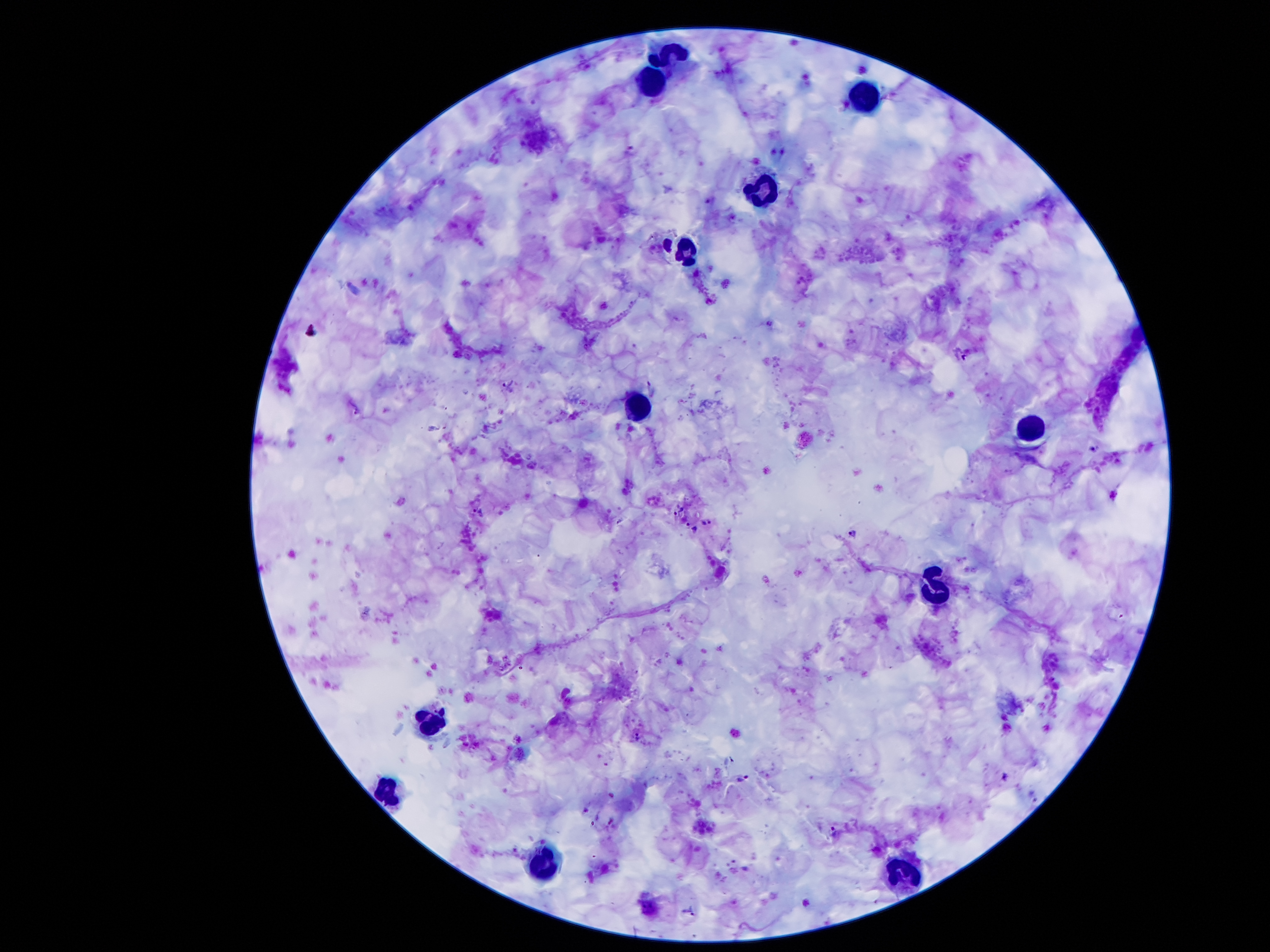

Approximate centers as (x, y) in pixels.
Summary:
  - Plasmodium parasite locations: (631, 151), (966, 353), (510, 386), (356, 407), (1094, 448), (677, 507), (478, 512), (621, 520), (707, 523), (692, 527), (854, 534), (637, 735), (744, 780), (835, 832), (692, 912)
  - Leukocyte locations: (666, 55), (647, 84), (861, 88), (763, 197), (687, 258), (639, 403), (1027, 418), (935, 592), (424, 722), (389, 798), (550, 865), (910, 876)
  - Stain: Giemsa
  - Image size: 1270×952 pixels
  - Capture: smartphone through the microscope eyepiece
  - Preparation: thick blood smear
  - Magnification: 100x
  - Patient malaria status: positive for Plasmodium falciparum
  - Field of view: single